Comment on the morphology of the red blood cells.
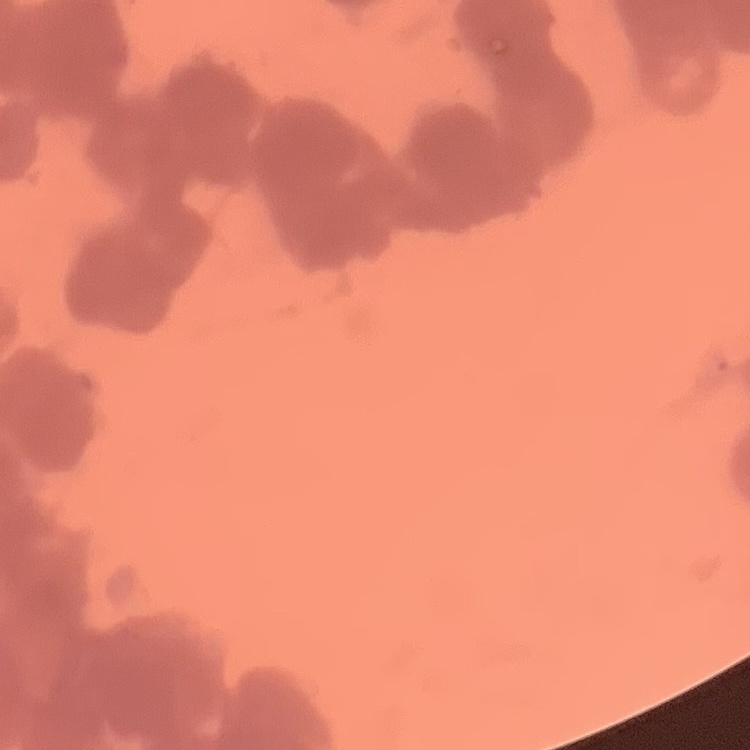

Rouleaux formation.

One tile cut from a larger photomicrograph. Thin peripheral smear. Stained with either Field's or Giemsa.